Give the preparation type.
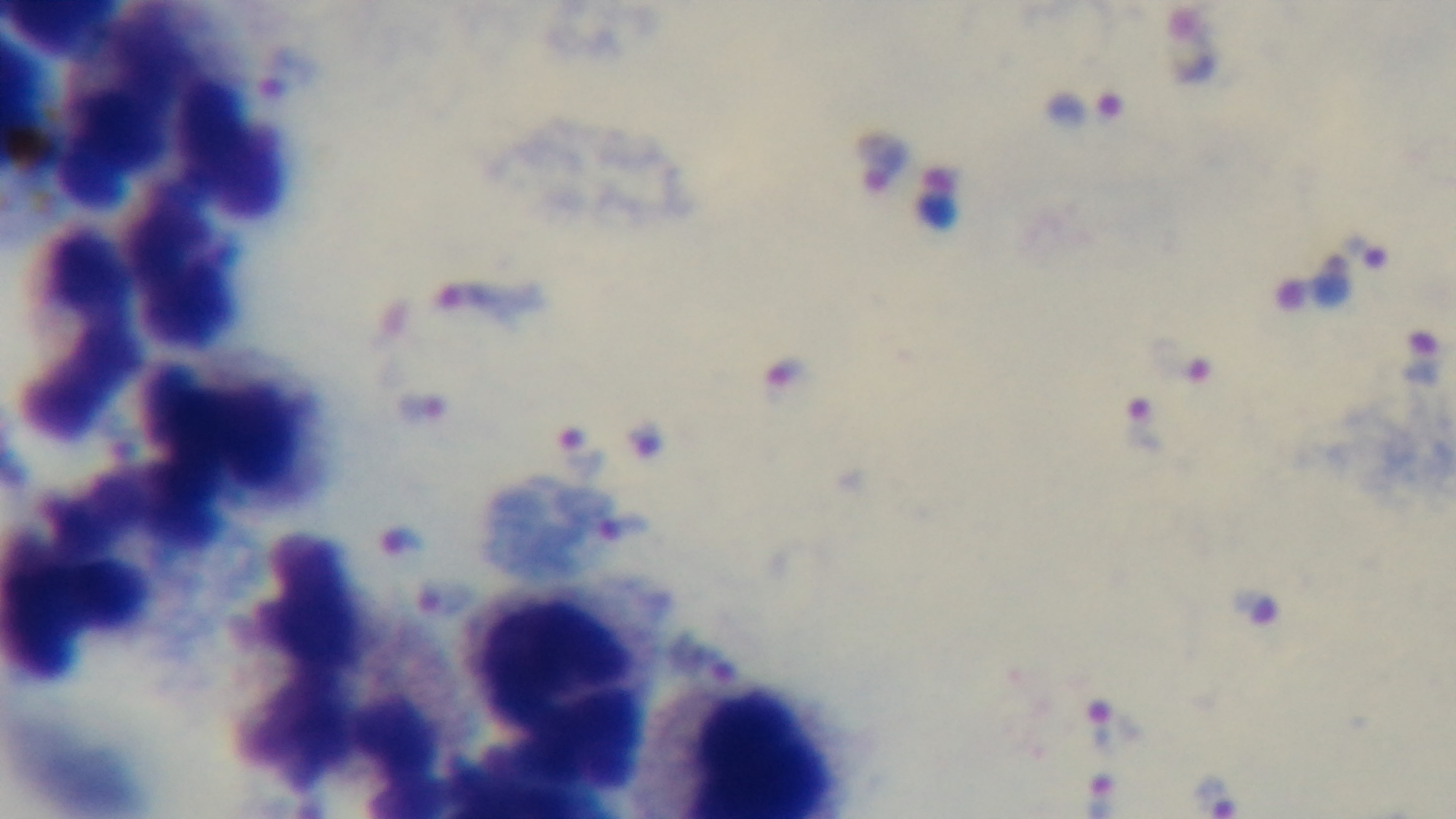
A thick smear.

objective: 100x oil immersion
field_of_view: single
malaria_status: infected
stain: Giemsa
capture: mounted 4K digital camera
modality: light microscopy